Locate every uninfected red blood cell.
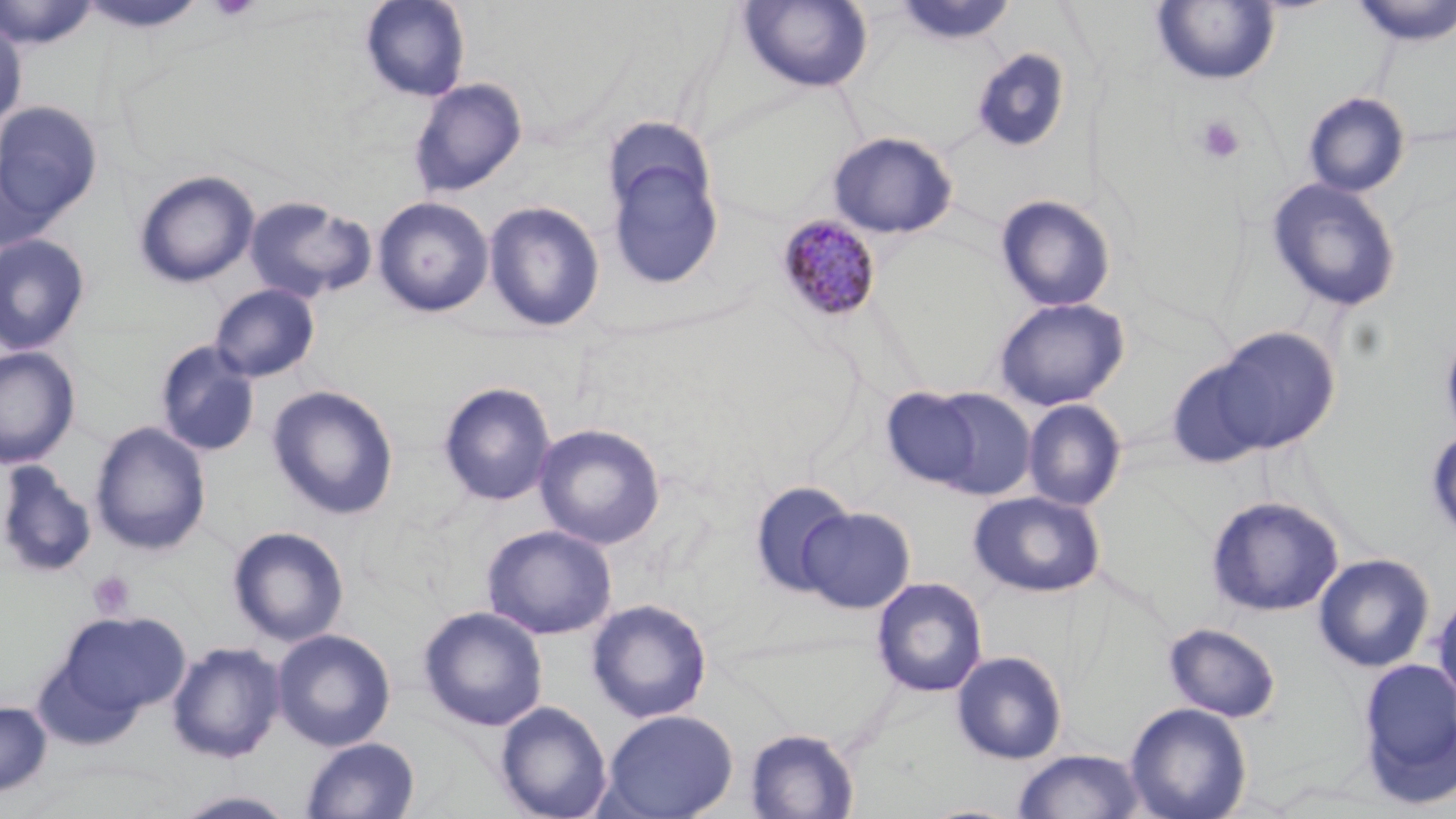

Approximate bounding boxes as named x1/y1/x2/y2 corners in pixels.
Uninfected red blood cells: (x1=0, y1=0, x2=99, y2=50), (x1=359, y1=0, x2=471, y2=102), (x1=1348, y1=0, x2=1455, y2=47), (x1=75, y1=1, x2=209, y2=35), (x1=737, y1=1, x2=874, y2=93), (x1=892, y1=1, x2=1019, y2=47), (x1=1150, y1=1, x2=1281, y2=87), (x1=0, y1=17, x2=27, y2=131), (x1=970, y1=49, x2=1071, y2=152), (x1=409, y1=78, x2=527, y2=198), (x1=1302, y1=91, x2=1411, y2=197), (x1=0, y1=101, x2=102, y2=227), (x1=601, y1=116, x2=715, y2=227), (x1=828, y1=131, x2=957, y2=239), (x1=603, y1=141, x2=725, y2=291), (x1=1, y1=151, x2=63, y2=257), (x1=134, y1=170, x2=260, y2=288), (x1=1266, y1=178, x2=1402, y2=312), (x1=994, y1=194, x2=1116, y2=312), (x1=243, y1=196, x2=376, y2=303), (x1=372, y1=196, x2=493, y2=317), (x1=484, y1=200, x2=605, y2=333), (x1=0, y1=234, x2=91, y2=355), (x1=210, y1=283, x2=320, y2=383), (x1=993, y1=297, x2=1130, y2=411), (x1=1439, y1=321, x2=1456, y2=447), (x1=1205, y1=327, x2=1340, y2=454), (x1=154, y1=340, x2=261, y2=457), (x1=0, y1=345, x2=80, y2=468), (x1=1164, y1=354, x2=1278, y2=470), (x1=438, y1=381, x2=557, y2=507), (x1=267, y1=385, x2=399, y2=520), (x1=880, y1=385, x2=990, y2=491), (x1=914, y1=387, x2=1038, y2=499), (x1=1022, y1=399, x2=1127, y2=511), (x1=90, y1=421, x2=211, y2=555), (x1=533, y1=423, x2=666, y2=549), (x1=1426, y1=427, x2=1456, y2=541), (x1=0, y1=463, x2=96, y2=578), (x1=749, y1=481, x2=856, y2=598), (x1=968, y1=490, x2=1105, y2=598), (x1=1206, y1=496, x2=1345, y2=618), (x1=798, y1=506, x2=915, y2=613), (x1=482, y1=524, x2=617, y2=639), (x1=228, y1=526, x2=349, y2=646), (x1=1313, y1=553, x2=1435, y2=672), (x1=870, y1=577, x2=988, y2=698), (x1=1431, y1=592, x2=1456, y2=710), (x1=587, y1=598, x2=712, y2=723), (x1=418, y1=606, x2=548, y2=731), (x1=55, y1=611, x2=190, y2=720), (x1=1163, y1=623, x2=1282, y2=722), (x1=272, y1=628, x2=396, y2=751), (x1=166, y1=641, x2=285, y2=763), (x1=951, y1=650, x2=1068, y2=764), (x1=1356, y1=657, x2=1456, y2=806), (x1=495, y1=700, x2=612, y2=819), (x1=0, y1=701, x2=52, y2=798), (x1=1125, y1=702, x2=1252, y2=819), (x1=601, y1=709, x2=739, y2=819), (x1=744, y1=727, x2=860, y2=818), (x1=300, y1=736, x2=420, y2=818), (x1=1012, y1=749, x2=1147, y2=819), (x1=170, y1=790, x2=300, y2=819).

Platelet locations: (x1=208, y1=0, x2=260, y2=21), (x1=1194, y1=113, x2=1246, y2=164), (x1=87, y1=570, x2=136, y2=620). Plasmodium malariae-infected red blood cell locations: (x1=775, y1=214, x2=883, y2=323). Slide-level diagnosis: Plasmodium malariae. 1000x magnification. Light microscopy. Image is 1456×819 pixels. May-Grünwald-Giemsa-stained preparation. Thin blood smear. One field of a larger specimen.